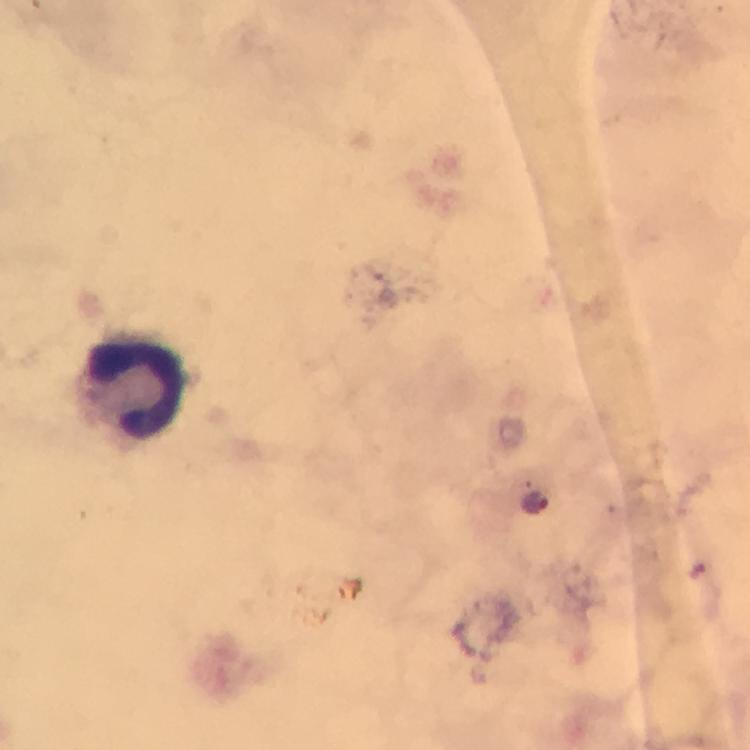
preparation = thick blood smear
malaria parasite locations = approximate centers as {x, y} in pixels: {531, 504}
immersion oil = used
capture = smartphone photograph through a microscope
leukocyte locations = approximate centers as {x, y} in pixels: {130, 385}
magnification = 100x
cropped from = a single field of view
image size = 750×750 pixels
context = from a malaria diagnostic workup
stain = Giemsa